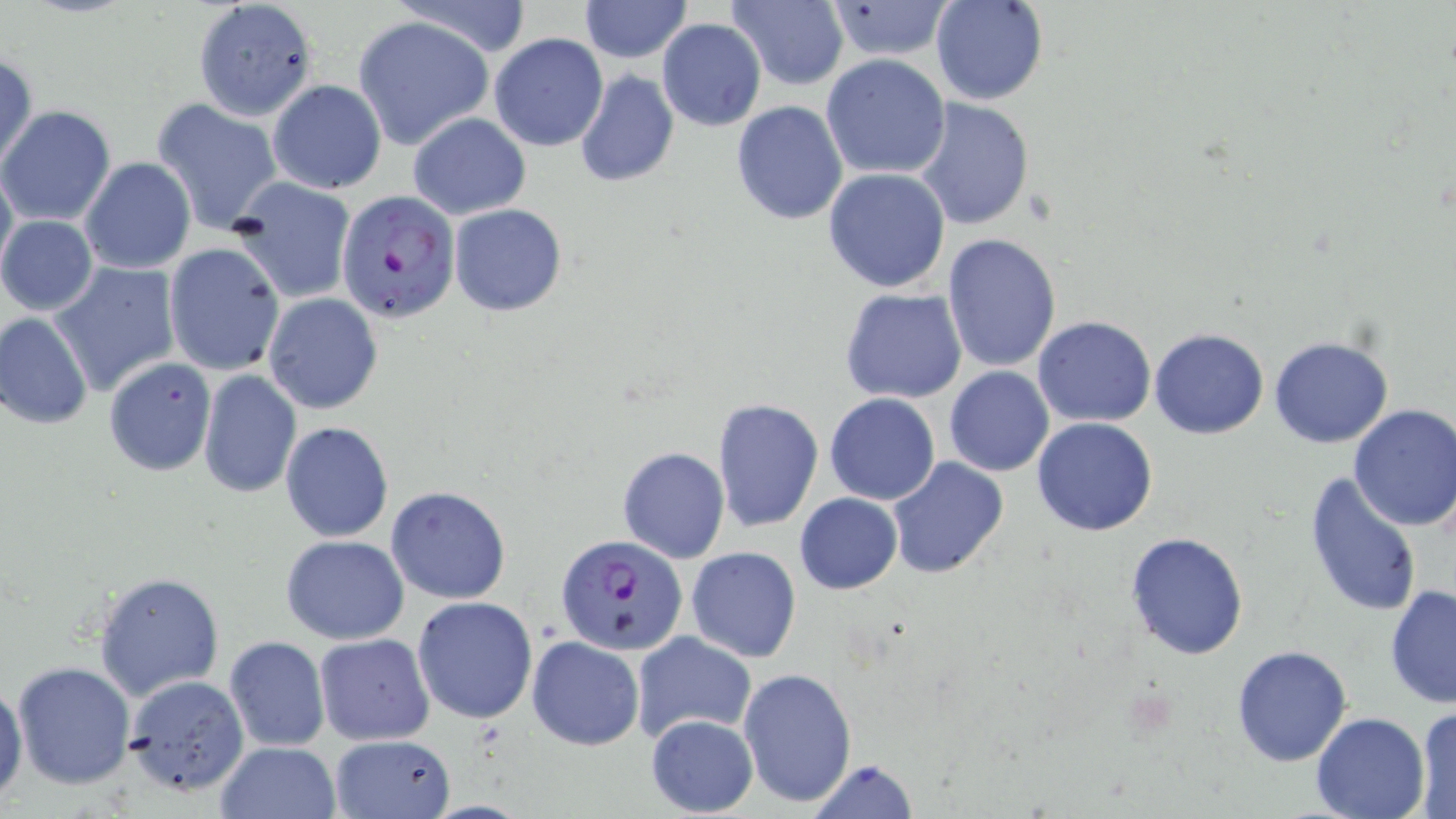 Approximate bounding boxes as (x1, y1, x2, y2) in pixels. Uninfected red blood cell locations: (391, 0, 532, 58), (579, 0, 690, 62), (727, 0, 849, 89), (931, 0, 1049, 106), (827, 1, 954, 60), (198, 2, 320, 123), (356, 17, 494, 148), (656, 19, 767, 132), (490, 33, 608, 152), (1, 50, 37, 174), (820, 53, 951, 179), (575, 69, 680, 189), (269, 80, 386, 195), (151, 97, 282, 233), (914, 98, 1034, 231), (731, 100, 848, 224), (1, 105, 116, 227), (409, 112, 530, 219), (0, 157, 17, 282), (80, 157, 195, 274), (823, 167, 951, 294), (231, 177, 356, 303), (449, 203, 567, 316), (1, 215, 99, 316), (942, 233, 1061, 373), (163, 242, 285, 376), (51, 262, 181, 396), (839, 288, 968, 405), (263, 293, 383, 414), (1, 313, 94, 429), (1033, 315, 1156, 427), (1149, 326, 1269, 439), (1269, 336, 1394, 449), (103, 357, 217, 475), (944, 365, 1054, 477), (196, 369, 302, 498), (825, 393, 941, 506), (713, 397, 824, 533), (1346, 405, 1456, 533), (1031, 417, 1159, 536), (280, 421, 394, 542), (617, 447, 729, 563), (886, 453, 1010, 578), (1303, 472, 1424, 619), (385, 486, 510, 604), (795, 492, 903, 595), (1124, 531, 1248, 660), (280, 536, 409, 644), (686, 546, 801, 663), (94, 572, 224, 701), (1384, 585, 1456, 708), (412, 596, 538, 723), (632, 629, 755, 742), (313, 633, 434, 745), (224, 635, 330, 752), (527, 636, 644, 750), (1231, 644, 1354, 767), (12, 661, 136, 789), (738, 668, 856, 808), (124, 675, 249, 796), (0, 681, 26, 802), (1413, 705, 1455, 817), (1310, 712, 1430, 819), (646, 713, 759, 815), (328, 734, 458, 818), (214, 741, 340, 819), (803, 760, 918, 819). Plasmodium falciparum-infected red blood cell locations: (337, 188, 461, 324), (556, 534, 687, 654). Slide-level diagnosis: Plasmodium falciparum. Single field of view. Thin blood smear. Light microscopy. May-Grünwald-Giemsa-stained preparation. Captured at 1000x magnification. Image is 1456×819 pixels.